Give the preparation type.
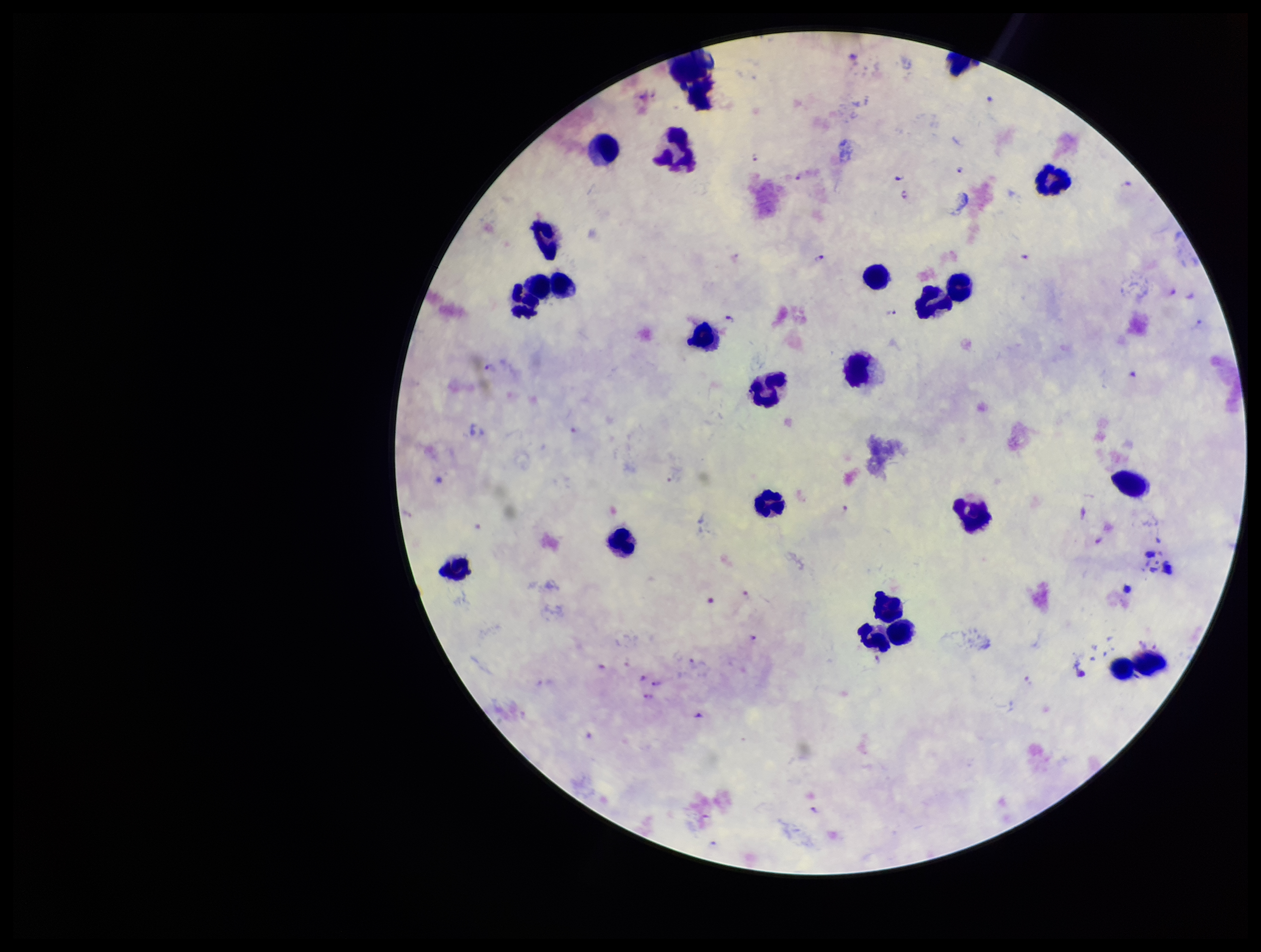

Thick.

capture: smartphone photograph through the microscope eyepiece
leukocyte_count: 24
image_size: 1261×952 pixels
species_reported_for_this_patient: Plasmodium falciparum
patient_malaria_status: positive
stain: Giemsa
field_of_view: single
parasite_count: 18
plasmodium_parasites: identified